Give the preparation type.
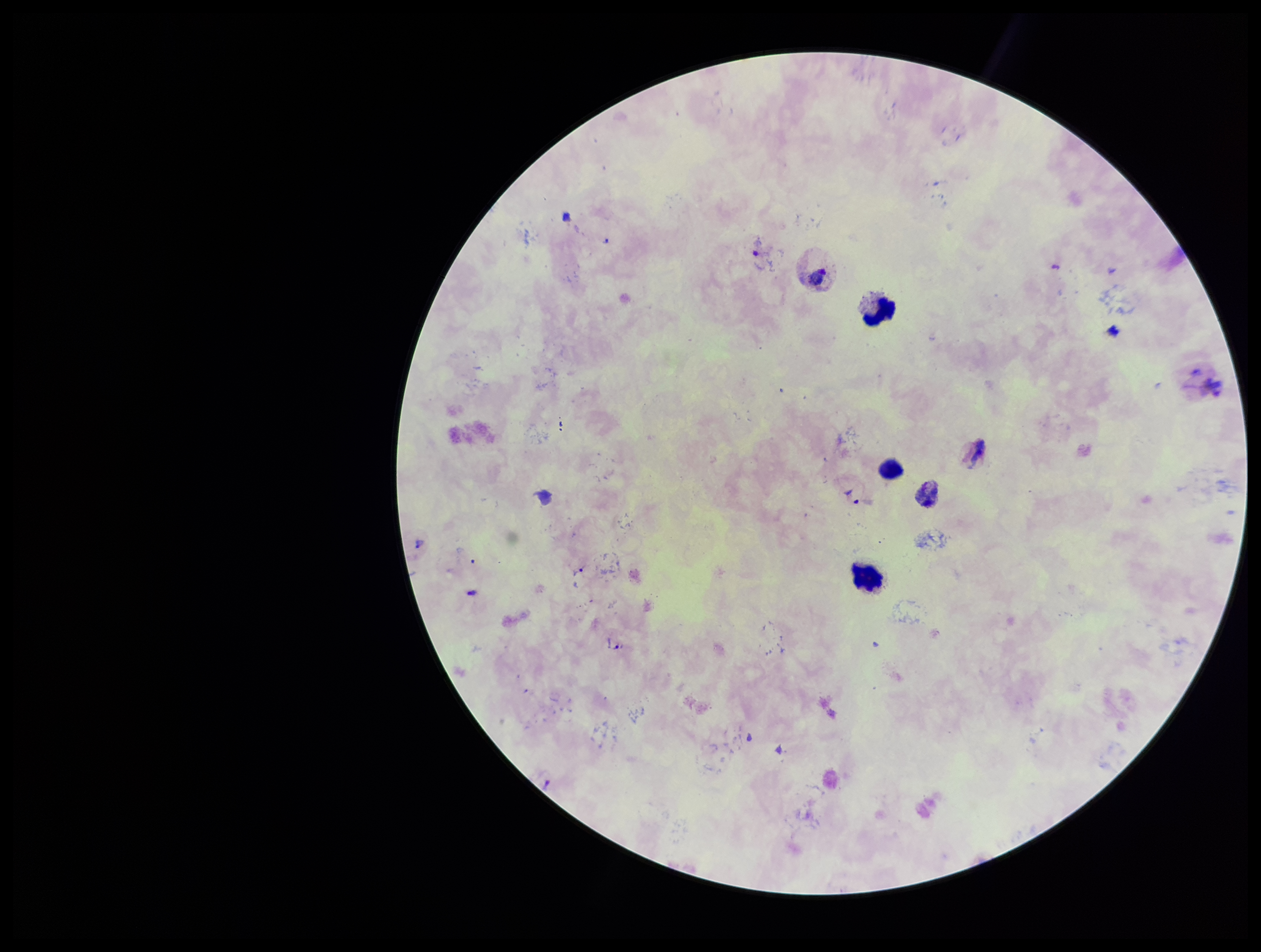
It is a thick blood smear.

parasite count = 5
capture = smartphone photograph through the microscope eyepiece
stain = Giemsa
Plasmodium parasites = identified
image size = 1261×952 pixels
species reported for this patient = Plasmodium vivax
patient malaria status = infected
leukocyte count = 4
field of view = one from this slide